Comment on the morphology of the erythrocytes.
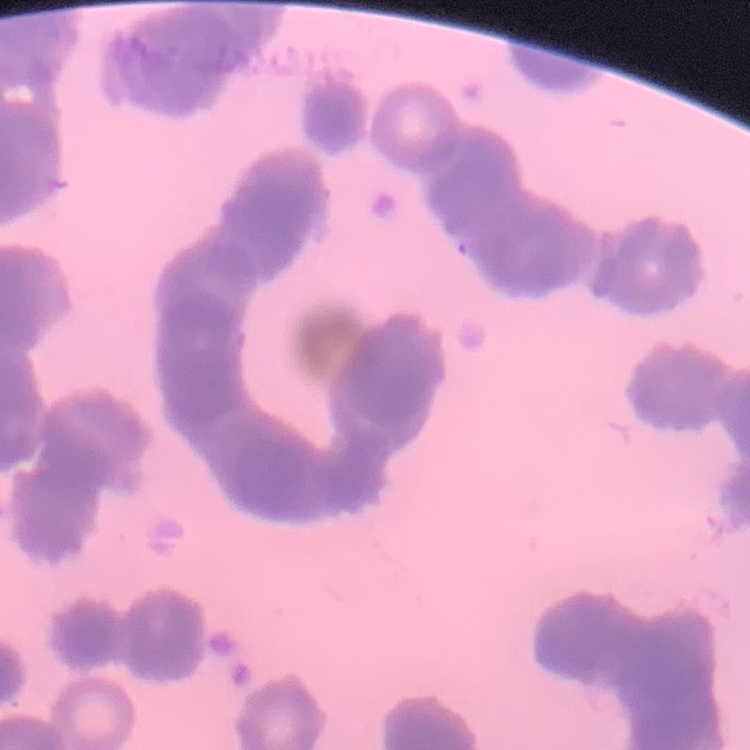
Rouleaux formation.

Summary:
  - Stain: Field's or Giemsa
  - Image type: one tile cut from a larger photomicrograph
  - Preparation: thin peripheral smear